Name the parasite shown.
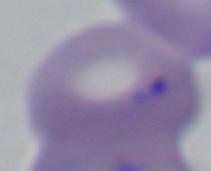
This is Babesia.

Micrograph. Captured at 1000x magnification.